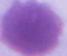

{
  "identification": "red blood cell",
  "modality": "micrograph",
  "magnification": "1000x"
}